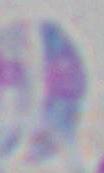
identification: Toxoplasma gondii
magnification: 1000x
modality: photomicrograph